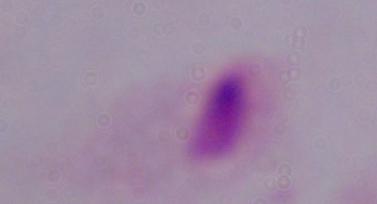
modality = micrograph
magnification = 1000x
identification = trichomonad